Outline each blood parasite and name the species.
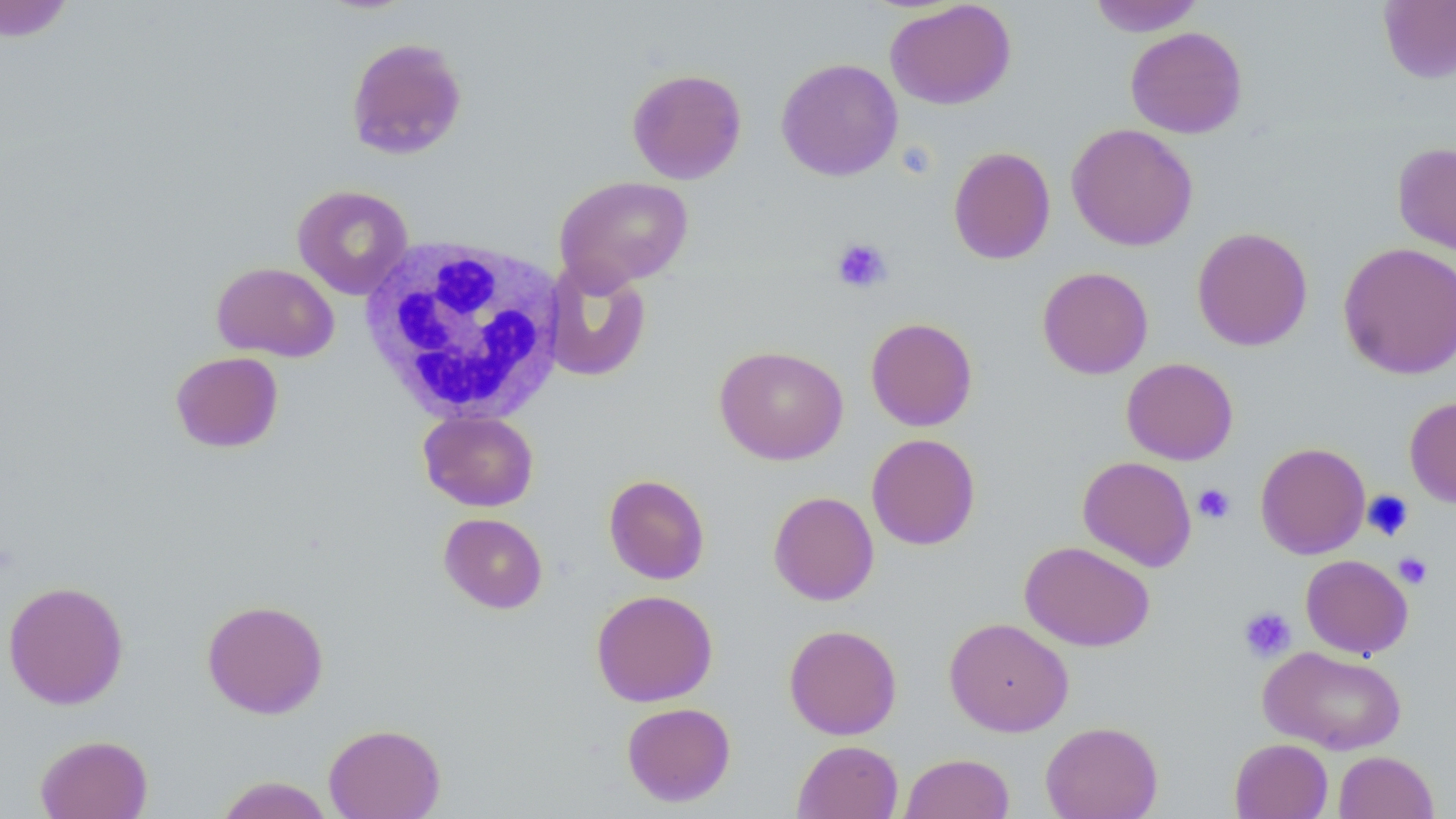

No blood parasites seen.

Summary:
  - Coordinate format: approximate bounding boxes as (x1, y1, x2, y2) in pixels
  - White blood cell locations: (357, 235, 570, 424)
  - Uninfected red blood cell locations: (0, 0, 75, 42), (1088, 0, 1205, 36), (1379, 0, 1456, 84), (885, 1, 1016, 110), (1125, 26, 1247, 139), (346, 37, 469, 160), (776, 58, 902, 182), (627, 67, 747, 184), (1066, 122, 1198, 252), (1392, 142, 1456, 255), (948, 146, 1055, 265), (554, 175, 693, 291), (293, 184, 414, 299), (1192, 226, 1313, 351), (1338, 242, 1456, 380), (211, 261, 339, 362), (542, 261, 653, 382), (1037, 266, 1153, 379), (865, 317, 978, 431), (714, 344, 849, 465), (170, 351, 284, 453), (1121, 358, 1238, 465), (1405, 396, 1456, 509), (418, 410, 539, 512), (866, 433, 981, 550), (1255, 441, 1370, 559), (1077, 456, 1197, 572), (603, 474, 710, 585), (768, 491, 880, 605), (439, 513, 548, 614), (1019, 541, 1155, 651), (1300, 554, 1413, 658), (3, 580, 129, 710), (591, 589, 718, 707), (202, 599, 329, 719), (944, 617, 1074, 737), (783, 624, 902, 740), (1258, 645, 1407, 755), (621, 701, 736, 807), (1040, 721, 1163, 819), (323, 722, 446, 819), (35, 734, 153, 819), (1229, 738, 1333, 819), (792, 740, 904, 819), (1333, 750, 1438, 819), (900, 752, 1015, 819), (215, 776, 334, 818)
  - Platelet locations: (831, 237, 892, 293), (1193, 483, 1236, 524), (1362, 490, 1415, 542), (1393, 552, 1433, 589), (1238, 606, 1296, 662)
  - Slide-level diagnosis: negative for blood parasites
  - Field of view: single
  - Magnification: 1000x
  - Stain: May-Grünwald-Giemsa
  - Preparation: thin blood smear
  - Image size: 1456×819 pixels
  - Modality: light microscopy